Name the parasite shown.
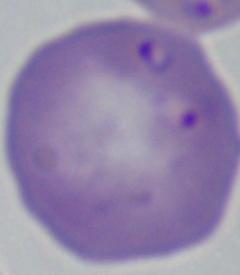
This is Babesia.

Summary:
  - Modality: photomicrograph
  - Magnification: 1000x